Report the malaria status of this cell.
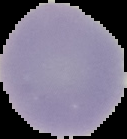

It is uninfected.

The area outside the segmented cell region is set to black. Image is 127×139 pixels. From a thin blood film.